Describe the morphology of the erythrocytes.
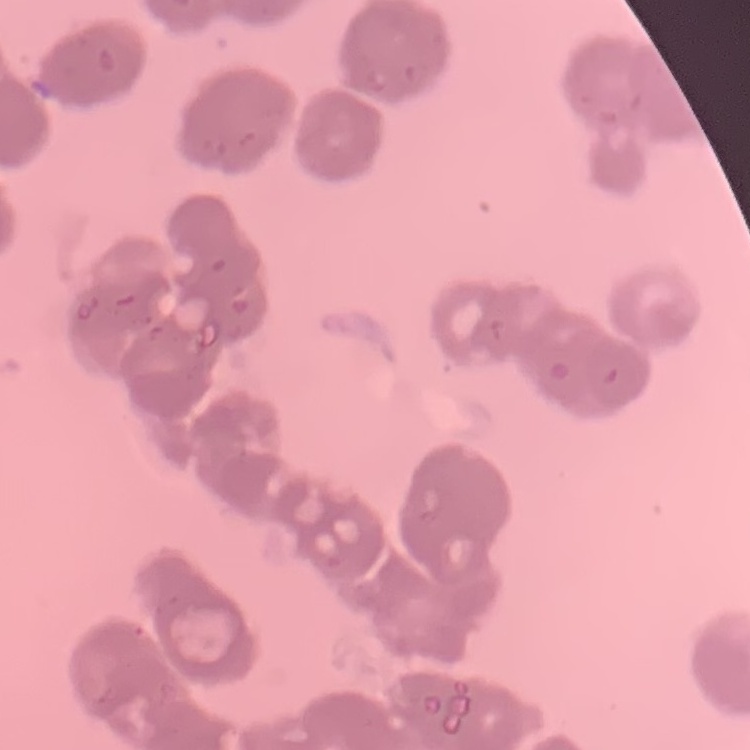

Rouleaux formation.

One tile cut from a larger photomicrograph. Thin peripheral smear. Stained with either Field's or Giemsa.